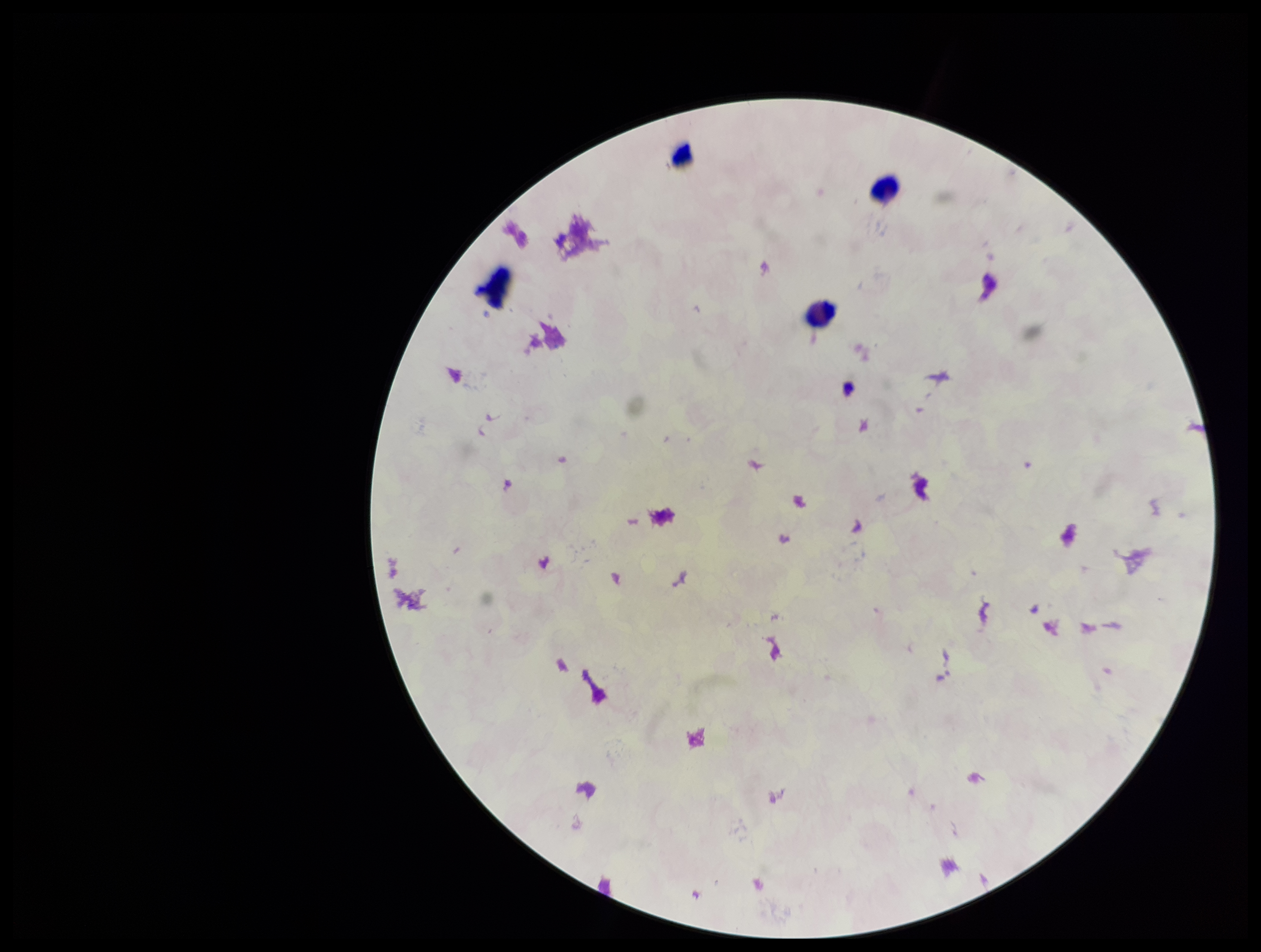

image size = 1261×952 pixels
Plasmodium parasites = none detected
patient malaria status = negative
field of view = single
capture = smartphone photograph through the microscope eyepiece
stain = Giemsa
leukocyte count = 3
parasite count = 0
preparation = thick